Report the malaria status of this cell.
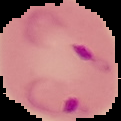
Parasitized.

Summary:
  - Image type: cell region segmented out of the field of view; surrounding area masked to black
  - Image size: 121×121 pixels
  - Preparation: thin blood film